Give the extent of all Plasmodium vivax-infected red blood cells.
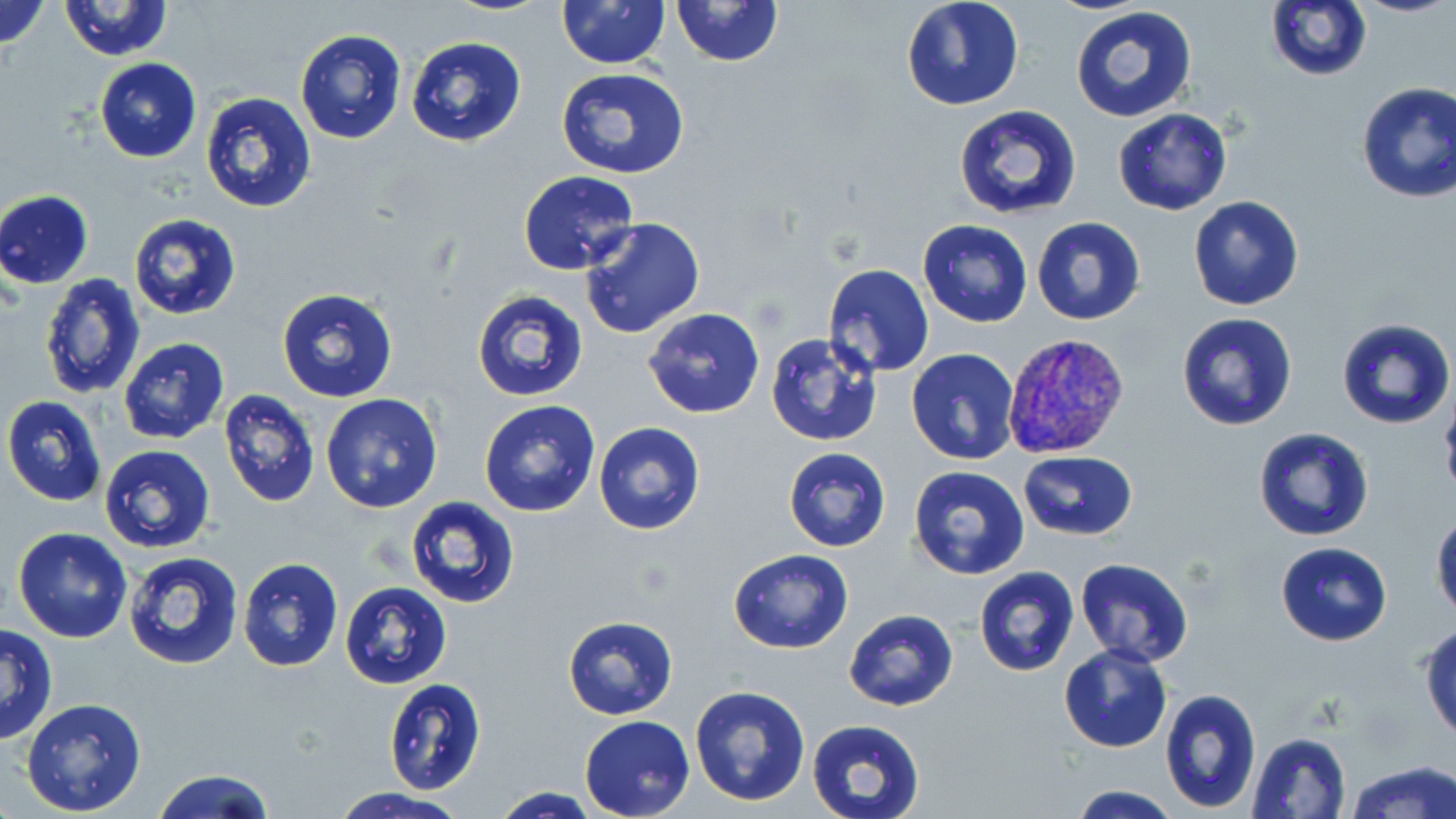
Approximate bounding boxes as [x1, y1, x2, y2] in pixels.
Plasmodium vivax-infected red blood cells: [1002, 332, 1130, 461].

slide-level diagnosis = Plasmodium vivax
image size = 1456×819 pixels
uninfected red blood cell locations = approximate bounding boxes as [x1, y1, x2, y2] in pixels: [0, 0, 51, 52], [671, 0, 783, 67], [901, 0, 1023, 110], [58, 1, 175, 61], [556, 1, 670, 69], [1264, 1, 1371, 81], [1068, 5, 1200, 125], [295, 30, 408, 143], [238, 34, 372, 164], [405, 35, 528, 149], [95, 58, 201, 162], [557, 67, 692, 180], [1354, 82, 1456, 204], [200, 91, 316, 213], [952, 105, 1082, 222], [1112, 107, 1233, 216], [517, 170, 638, 276], [0, 190, 93, 288], [1188, 195, 1304, 311], [128, 213, 242, 320], [580, 216, 704, 339], [1032, 216, 1146, 325], [918, 218, 1033, 328], [823, 263, 934, 377], [39, 273, 145, 398], [276, 286, 400, 404], [472, 289, 590, 402], [642, 308, 764, 419], [1176, 311, 1299, 431], [1336, 316, 1454, 430], [764, 332, 886, 447], [118, 337, 231, 445], [906, 349, 1019, 464], [218, 389, 320, 506], [320, 392, 446, 513], [1439, 392, 1456, 505], [3, 395, 106, 506], [478, 400, 601, 519], [593, 422, 704, 535], [1253, 426, 1374, 541], [97, 445, 215, 553], [784, 446, 891, 551], [1018, 451, 1138, 541], [909, 465, 1030, 579], [405, 495, 521, 608], [1430, 510, 1456, 622], [12, 528, 133, 643], [1275, 542, 1392, 646], [728, 549, 853, 654], [123, 550, 244, 671], [238, 557, 344, 672], [1076, 558, 1195, 668], [973, 566, 1080, 676], [338, 581, 453, 689], [844, 609, 958, 711], [563, 615, 678, 720], [0, 623, 59, 744], [1420, 623, 1455, 742], [1059, 644, 1171, 753], [383, 678, 487, 794], [689, 683, 813, 806], [1159, 686, 1260, 813], [21, 697, 147, 816], [579, 715, 695, 819], [807, 718, 926, 819], [1247, 732, 1351, 819], [1345, 760, 1455, 818], [151, 768, 276, 819], [1066, 785, 1185, 818], [490, 787, 601, 818], [328, 788, 471, 819]
stain = May-Grünwald-Giemsa
preparation = thin blood film
magnification = 1000x
modality = optical microscopy
field of view = single